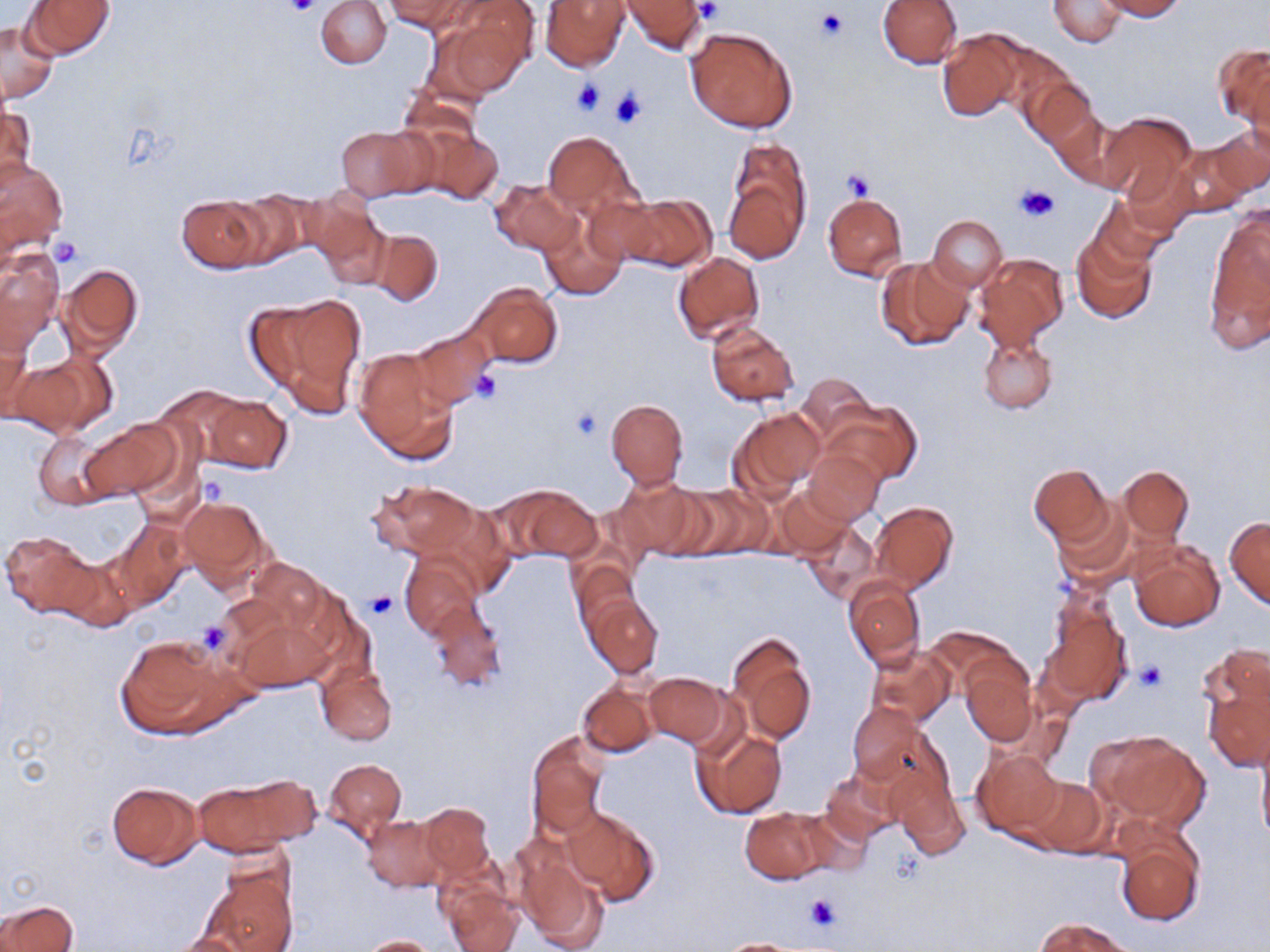
Approximate bounding boxes as (x1,y1)-(x2,y2) corner pairs in pixels. Uninfected red blood cell locations: (316,0)-(392,69), (387,0)-(473,34), (542,0)-(630,70), (620,0)-(708,54), (1048,0)-(1127,48), (1099,0)-(1185,20), (24,1)-(115,58), (437,1)-(536,99), (877,1)-(960,69), (1,21)-(57,104), (685,26)-(798,133), (938,29)-(1023,122), (1215,44)-(1269,132), (1022,76)-(1098,152), (1,105)-(35,186), (1054,111)-(1133,192), (1096,111)-(1197,205), (1210,123)-(1270,197), (414,124)-(504,207), (335,125)-(428,199), (543,130)-(639,219), (723,139)-(812,261), (1173,144)-(1253,216), (0,156)-(69,255), (489,178)-(582,255), (822,192)-(907,281), (222,193)-(311,267), (611,193)-(717,272), (178,197)-(266,272), (1092,199)-(1174,271), (306,201)-(391,285), (1206,209)-(1270,343), (539,210)-(629,299), (927,215)-(1008,290), (369,228)-(443,306), (1071,233)-(1158,326), (1,249)-(63,350), (673,252)-(764,342), (974,253)-(1068,350), (876,256)-(973,352), (58,264)-(143,357), (469,283)-(562,370), (248,294)-(367,415), (0,321)-(34,417), (706,322)-(798,407), (408,326)-(494,411), (978,333)-(1058,414), (353,349)-(459,464), (11,352)-(112,436), (795,375)-(876,447), (203,395)-(293,474), (606,399)-(689,489), (824,401)-(921,485), (732,407)-(825,498), (82,422)-(179,499), (34,431)-(113,511), (805,448)-(884,525), (1028,464)-(1112,545), (1119,466)-(1194,542), (610,476)-(701,561), (370,481)-(478,559), (502,484)-(604,563), (777,485)-(852,558), (670,486)-(768,560), (178,495)-(273,592), (1052,498)-(1137,587), (871,501)-(959,591), (1225,516)-(1270,609), (110,520)-(190,607), (801,522)-(879,604), (1,530)-(97,616), (1130,540)-(1225,632), (401,554)-(482,638), (57,556)-(139,633), (249,559)-(328,636), (570,561)-(640,637), (844,576)-(925,669), (1041,588)-(1132,708), (585,595)-(662,677), (426,599)-(507,693), (234,617)-(330,693), (726,632)-(816,745), (115,636)-(231,738), (865,644)-(954,727), (1197,647)-(1270,768), (962,660)-(1038,746), (316,662)-(396,745), (643,673)-(729,748), (577,682)-(659,757), (847,703)-(925,785), (691,726)-(787,819), (1257,729)-(1270,850), (526,731)-(608,841), (1096,732)-(1210,829), (973,748)-(1062,839), (325,758)-(406,840), (888,762)-(969,860), (819,767)-(902,847), (1022,773)-(1108,856), (189,776)-(309,859), (105,781)-(203,868), (418,802)-(494,880), (562,807)-(660,905), (739,807)-(834,882), (361,815)-(449,893), (1114,823)-(1205,928), (512,843)-(609,951), (197,866)-(299,952), (438,878)-(521,952), (0,900)-(77,952), (1035,917)-(1135,951), (171,932)-(255,952), (359,935)-(442,952), (712,939)-(814,951). Platelet locations: (283,0)-(322,17), (695,2)-(723,24), (815,8)-(848,42), (571,77)-(607,116), (610,87)-(648,129), (842,169)-(877,200), (1016,183)-(1060,223), (52,237)-(84,266), (471,371)-(504,405), (569,406)-(603,442), (197,478)-(228,509), (366,592)-(398,619), (194,619)-(232,655), (1134,662)-(1168,693), (804,892)-(842,932). Slide-level diagnosis: no evidence of blood parasites. Thin blood smear. Light microscopy. Captured at 1000x magnification. One field of a larger specimen. May-Grünwald-Giemsa-stained preparation. Image is 1270×952 pixels.